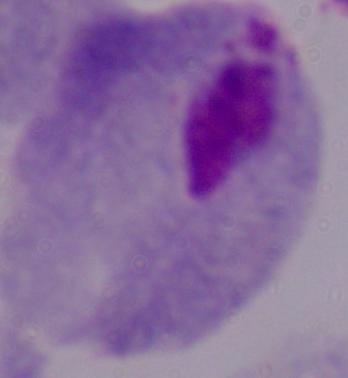
Summary:
  - Identification: trichomonad
  - Modality: photomicrograph
  - Magnification: 1000x